Describe the morphology of the red blood cells.
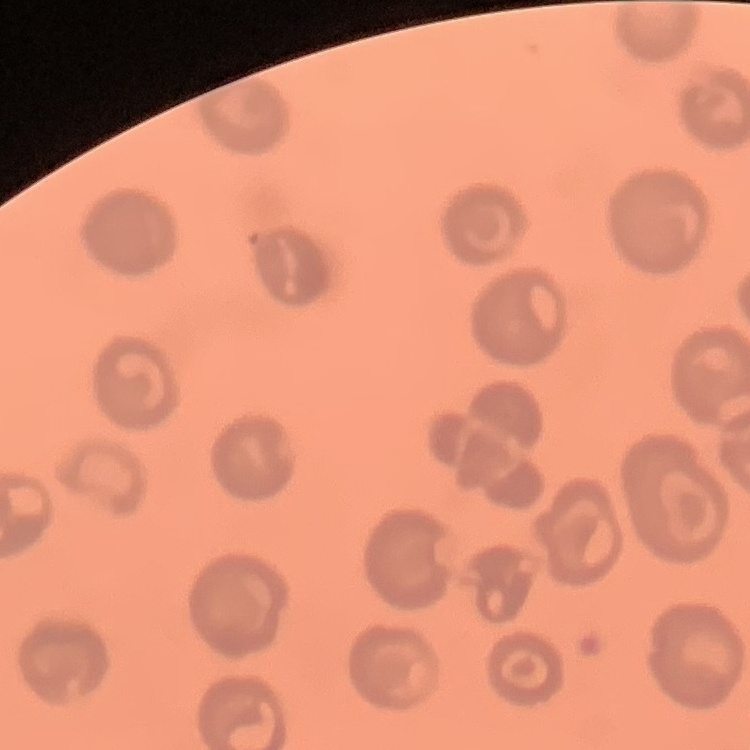

No rouleaux formation.

Field's or Giemsa stain. Thin blood film. One tile cut from a larger photomicrograph.